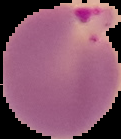

image size = 121×139 pixels
result = malaria parasites detected
preparation = thin blood smear
image type = segmented cell region with the area outside set to black